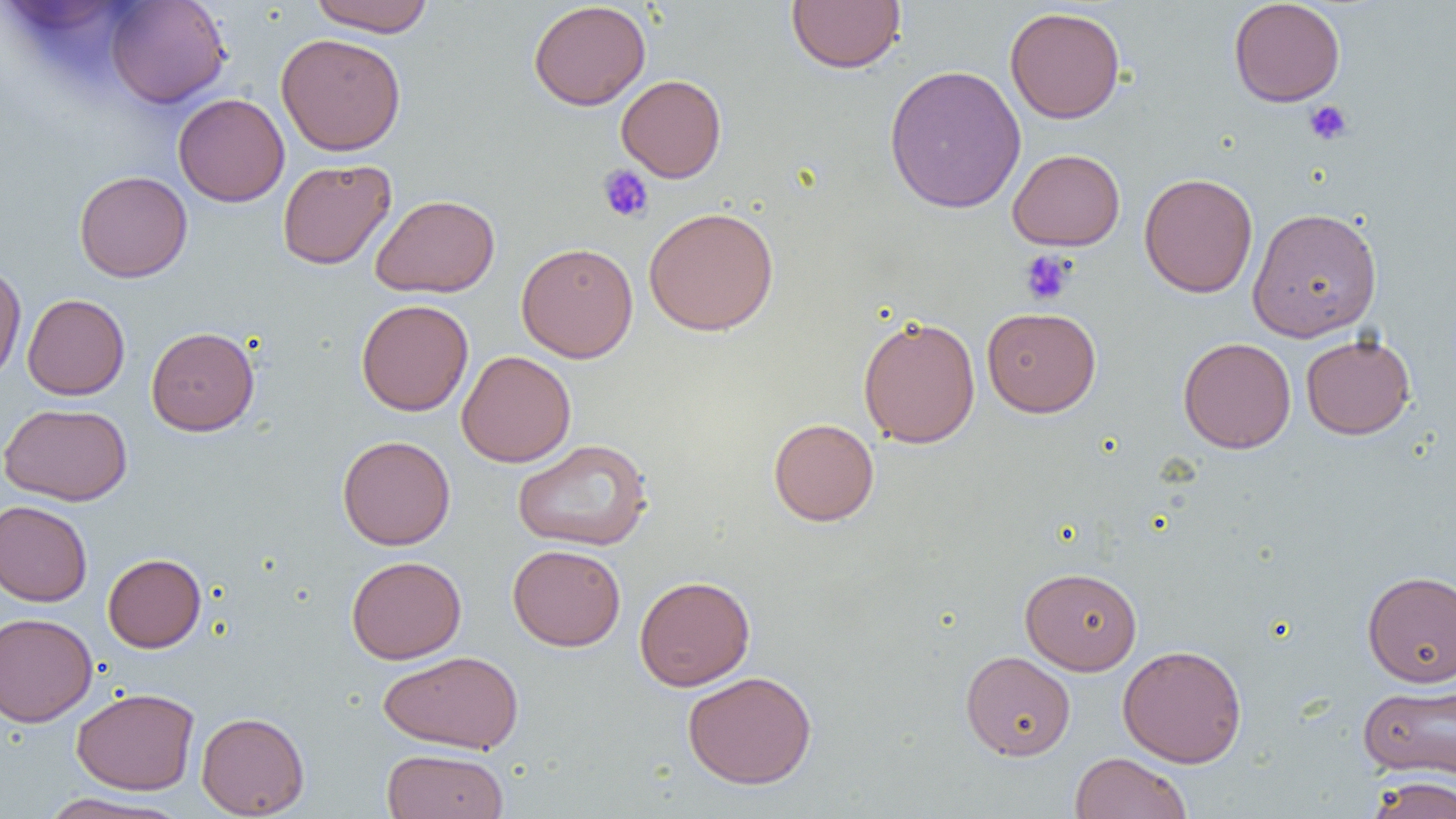

Summary:
  - Coordinate format: approximate bounding boxes as (x1, y1, x2, y2) in pixels
  - Uninfected red blood cell locations: (308, 0, 434, 36), (786, 0, 905, 73), (1228, 0, 1346, 107), (105, 1, 232, 108), (528, 1, 651, 110), (1005, 6, 1126, 123), (276, 32, 406, 156), (884, 64, 1026, 214), (616, 74, 727, 182), (174, 92, 290, 207), (1008, 148, 1125, 250), (277, 158, 396, 269), (74, 170, 192, 282), (1139, 172, 1258, 298), (370, 194, 500, 297), (644, 206, 779, 336), (1247, 207, 1383, 342), (516, 242, 639, 362), (0, 263, 27, 385), (22, 294, 130, 400), (356, 299, 473, 416), (981, 307, 1102, 417), (858, 314, 981, 448), (146, 326, 260, 435), (1301, 334, 1416, 439), (1178, 336, 1296, 453), (456, 350, 576, 467), (1, 402, 132, 506), (768, 418, 879, 526), (337, 435, 456, 550), (511, 438, 654, 552), (0, 500, 92, 607), (507, 543, 626, 651), (103, 553, 206, 652), (346, 555, 466, 663), (1020, 566, 1142, 675), (1362, 570, 1456, 687), (634, 575, 755, 691), (0, 612, 97, 726), (1117, 643, 1247, 767), (378, 650, 523, 754), (960, 650, 1076, 760), (682, 670, 817, 789), (1358, 683, 1455, 781), (71, 687, 199, 795), (196, 711, 310, 818), (381, 748, 509, 818), (1070, 752, 1192, 819), (1363, 776, 1456, 819), (37, 792, 188, 819)
  - Platelet locations: (1304, 100, 1353, 145), (597, 164, 655, 223), (1019, 251, 1075, 305)
  - Slide-level diagnosis: negative for blood parasites
  - Field of view: single
  - Preparation: thin blood smear
  - Magnification: 1000x
  - Image size: 1456×819 pixels
  - Modality: optical microscopy